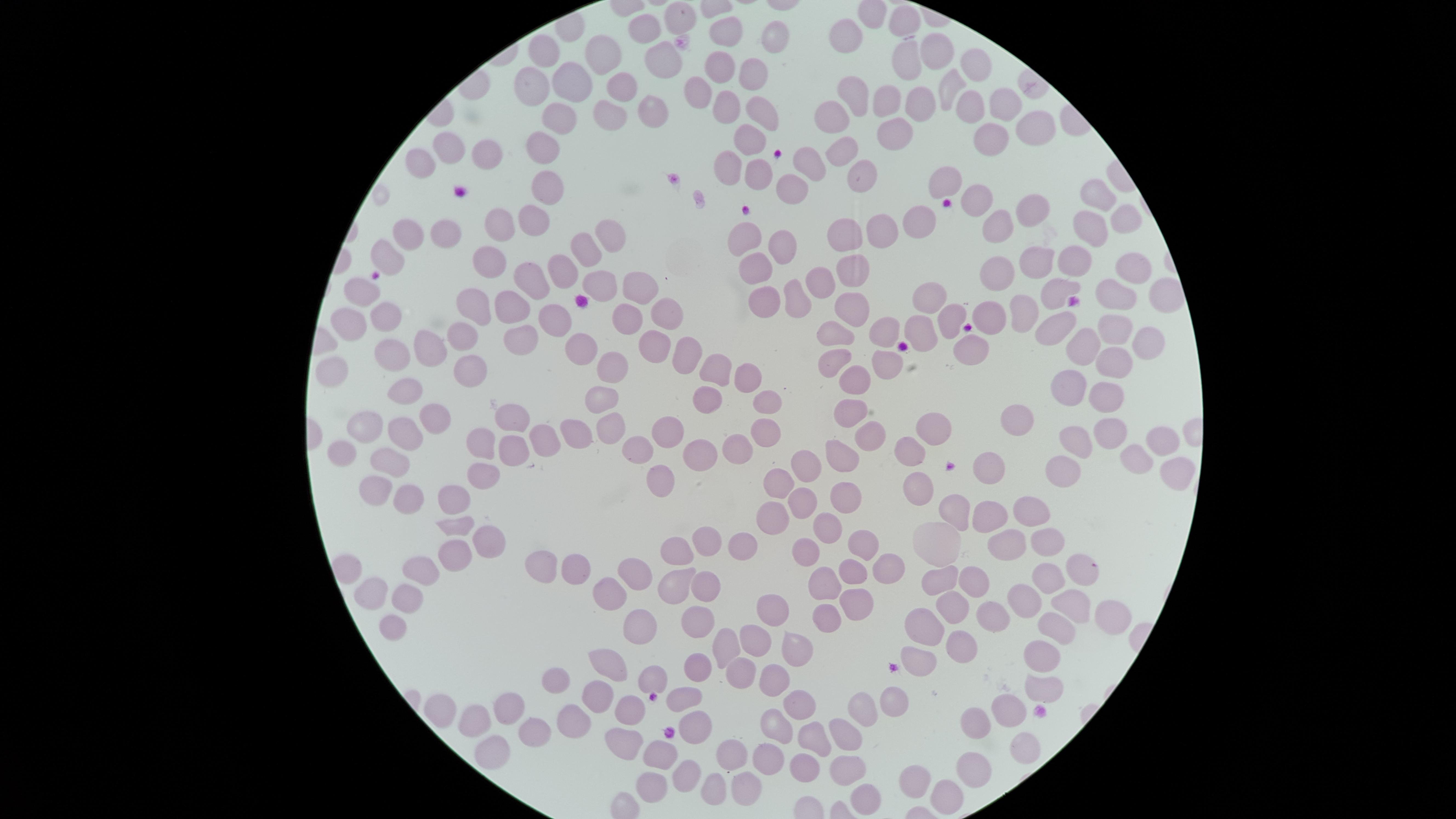
stain = Giemsa
presence = no malaria parasites detected
preparation = thin smear of blood
uninfected RBCs = approximate marker points as {x, y} in pixels: {907, 16}, {677, 17}, {648, 27}, {778, 32}, {850, 33}, {727, 34}, {935, 47}, {550, 49}, {608, 55}, {905, 57}, {663, 62}, {981, 63}, {718, 69}, {749, 70}, {580, 74}, {530, 80}, {619, 80}, {948, 85}, {699, 92}, {859, 98}, {889, 100}, {997, 101}, {724, 104}, {918, 105}, {644, 107}, {971, 107}, {755, 111}, {836, 115}, {562, 116}, {610, 116}, {1029, 125}, {891, 131}, {747, 138}, {993, 138}, {542, 144}, {847, 146}, {444, 148}, {487, 150}, {419, 159}, {800, 162}, {725, 165}, {862, 168}, {752, 173}, {943, 180}, {547, 184}, {794, 186}, {1096, 195}, {982, 196}, {1030, 206}, {537, 215}, {1122, 217}, {921, 219}, {505, 222}, {1000, 225}, {888, 228}, {1092, 229}, {612, 232}, {448, 234}, {405, 235}, {851, 237}, {741, 239}, {780, 243}, {591, 247}, {383, 254}, {491, 261}, {1082, 261}, {756, 263}, {562, 265}, {1038, 265}, {849, 267}, {1128, 268}, {1000, 275}, {598, 278}, {532, 281}, {813, 281}, {361, 284}, {628, 285}, {1059, 290}, {795, 295}, {930, 300}, {1115, 300}, {764, 303}, {515, 306}, {658, 308}, {383, 309}, {478, 309}, {857, 311}, {1022, 311}, {345, 313}, {986, 315}, {951, 316}, {554, 318}, {1111, 321}, {635, 325}, {1051, 328}, {842, 330}, {461, 333}, {886, 333}, {522, 336}, {923, 336}, {1148, 338}, {652, 344}, {427, 348}, {970, 348}, {1082, 351}, {577, 352}, {686, 352}, {839, 355}, {399, 356}, {878, 357}, {609, 359}, {1120, 361}, {457, 371}, {709, 372}, {735, 372}, {334, 374}, {854, 379}, {1075, 388}, {405, 392}, {1107, 393}, {599, 400}, {713, 400}, {765, 401}, {856, 412}, {1025, 414}, {514, 416}, {433, 419}, {932, 423}, {669, 426}, {758, 427}, {1108, 427}, {606, 429}, {362, 431}, {575, 433}, {1153, 433}, {403, 435}, {873, 437}, {486, 438}, {548, 438}, {1074, 441}, {737, 442}, {347, 449}, {511, 449}, {640, 449}, {911, 451}, {391, 458}, {843, 458}, {697, 460}, {1138, 460}, {812, 462}, {1067, 468}, {989, 469}, {1176, 471}, {484, 472}, {655, 473}, {781, 477}, {380, 487}, {914, 487}, {405, 494}, {447, 494}, {840, 500}, {801, 505}, {778, 511}, {1029, 514}, {959, 515}, {989, 517}, {454, 525}, {827, 525}, {479, 537}, {709, 543}, {738, 543}, {1008, 545}, {1044, 548}, {860, 550}, {677, 552}, {810, 552}, {450, 555}, {542, 565}, {345, 570}, {416, 570}, {575, 570}, {845, 572}, {1081, 573}, {640, 575}, {886, 575}, {945, 575}, {975, 576}, {820, 581}, {1051, 581}, {669, 587}, {706, 590}, {370, 593}, {609, 597}, {405, 598}, {850, 601}, {1027, 601}, {767, 603}, {955, 609}, {1069, 609}, {993, 614}, {818, 616}, {1110, 619}, {922, 621}, {394, 625}, {696, 625}, {1047, 629}, {637, 630}, {723, 643}, {754, 643}, {790, 652}, {952, 652}, {1044, 657}, {609, 659}, {917, 660}, {697, 664}, {738, 669}, {768, 679}, {650, 681}, {557, 682}, {1042, 690}, {686, 693}, {598, 698}, {442, 700}, {630, 702}, {890, 702}, {798, 703}, {865, 708}, {509, 709}, {1006, 710}, {471, 716}, {575, 718}, {688, 723}, {972, 724}, {776, 725}, {532, 730}, {849, 734}, {621, 738}, {815, 740}, {1021, 749}, {727, 754}, {485, 756}, {662, 757}, {769, 757}, {965, 766}, {804, 768}, {851, 771}, {686, 774}, {920, 777}, {646, 781}, {708, 784}, {749, 785}, {949, 796}, {862, 801}
image size = 1456×819 pixels
visible region = circular
field of view = single
capture = smartphone photograph through the microscope eyepiece